Assess the morphology of the red blood cells.
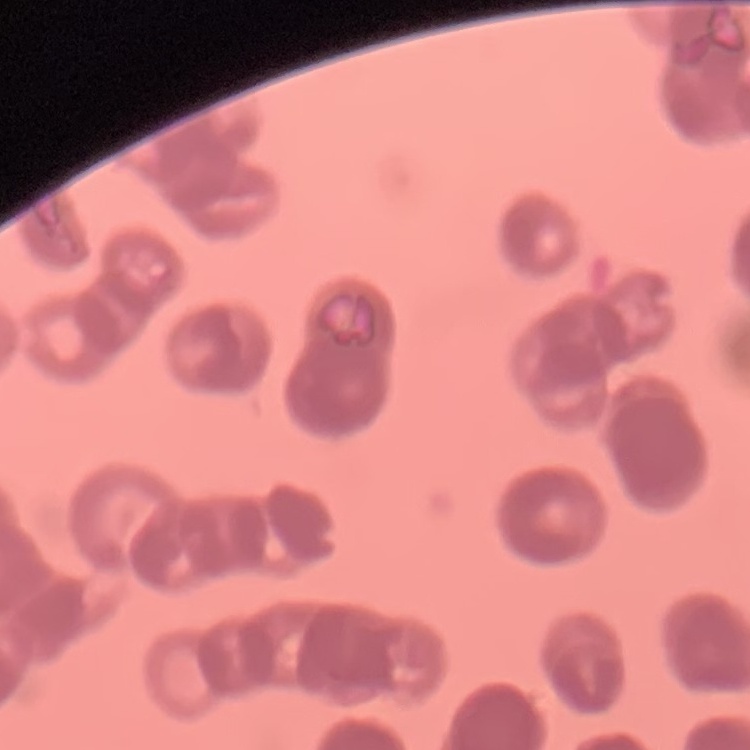
They show rouleaux formation.

Summary:
  - Preparation: thin blood smear
  - Stain: Field's or Giemsa
  - Image type: one tile cut from a larger photomicrograph